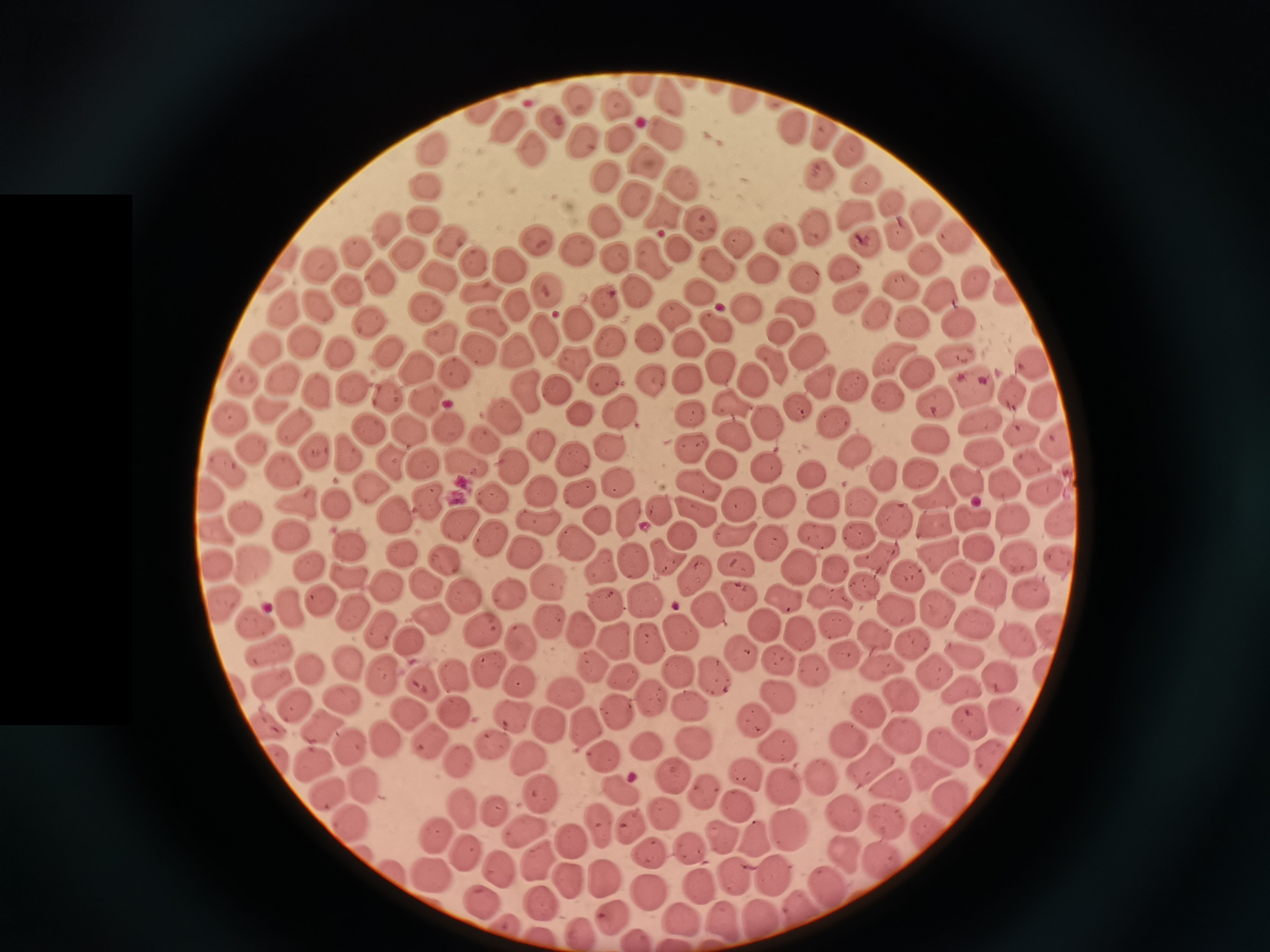

cell locations = approximate centers as (x, y) in pixels: (642, 82), (669, 97), (579, 98), (745, 102), (616, 105), (481, 108), (552, 118), (506, 124), (790, 127), (820, 130), (668, 133), (619, 139), (582, 140), (528, 145), (435, 149), (850, 151), (644, 162), (606, 175), (819, 176), (862, 177), (684, 178), (425, 187), (633, 196), (893, 204), (664, 212), (854, 215), (922, 216), (422, 220), (605, 220), (703, 221), (814, 224), (384, 228), (894, 233), (953, 238), (451, 240), (537, 242), (781, 242), (736, 243), (866, 243), (407, 246), (575, 248), (681, 248), (358, 251), (655, 258), (618, 259), (472, 261), (922, 261), (717, 262), (507, 263), (320, 265), (756, 265), (840, 270), (436, 274), (802, 278), (377, 279), (977, 285), (347, 286), (902, 286), (483, 290), (551, 290), (634, 291), (703, 291), (1007, 294), (942, 295), (605, 300), (849, 300), (517, 302), (747, 304), (315, 306), (428, 307), (285, 308), (797, 312), (674, 315), (878, 315), (485, 318), (371, 319), (959, 319), (915, 320), (579, 321), (718, 328), (780, 328), (542, 332), (444, 337), (651, 338), (306, 340), (683, 340), (610, 342), (389, 347), (519, 348), (270, 350), (480, 350), (343, 352), (809, 354), (955, 356), (892, 358), (769, 360), (572, 361), (418, 363), (1032, 363), (718, 364), (454, 368), (913, 371), (686, 376), (603, 378), (282, 380), (649, 380), (755, 380), (245, 381), (820, 381), (853, 386), (312, 387), (353, 388), (527, 388), (972, 388), (559, 390), (1012, 390), (886, 395), (384, 396), (1046, 396), (424, 397), (730, 401), (933, 404), (581, 409), (273, 411), (689, 411), (799, 411), (617, 413), (234, 415), (505, 418), (763, 420), (980, 422), (836, 423), (447, 427), (294, 428), (366, 428), (406, 430), (1020, 431), (732, 436), (489, 440), (689, 440), (539, 441), (607, 441), (936, 444), (1057, 447), (251, 449), (853, 451), (311, 453), (981, 453), (350, 456), (569, 457), (1027, 460), (460, 461), (393, 463), (422, 463), (512, 464), (720, 464), (766, 468), (227, 470), (281, 471), (917, 471), (810, 473), (885, 475), (964, 475), (614, 479), (698, 483), (370, 487), (1005, 487), (577, 489), (539, 490), (935, 494), (207, 495), (1044, 495), (491, 496), (776, 499), (431, 501), (294, 502), (739, 502), (863, 503), (335, 506), (659, 506), (696, 506), (821, 506), (398, 514), (628, 514), (596, 517), (245, 518), (536, 518), (894, 518), (1061, 518), (971, 519), (1014, 519), (932, 521), (458, 522), (215, 530), (861, 532), (733, 534), (287, 535), (683, 535), (817, 537), (492, 538), (573, 539), (765, 540), (348, 542), (977, 546), (524, 549), (937, 550), (666, 552), (1017, 552), (399, 553), (881, 557), (631, 558), (1058, 558), (441, 560), (253, 563), (304, 564), (602, 565), (732, 565), (217, 566), (798, 567), (833, 567), (904, 573), (693, 575), (962, 577), (353, 578), (546, 581), (422, 585), (387, 588), (994, 588), (508, 594), (733, 594), (641, 595), (781, 596), (460, 597), (1030, 598), (320, 599), (833, 599), (290, 604), (602, 604), (933, 605), (226, 607), (892, 609), (707, 611), (349, 612), (548, 620), (252, 623), (430, 623), (764, 623), (831, 623), (974, 626), (579, 627), (383, 628), (489, 629), (1050, 631), (678, 632), (798, 632), (646, 635), (412, 638), (875, 638), (523, 641), (616, 641), (1017, 641), (914, 648), (734, 651), (838, 651), (959, 652), (266, 655), (775, 658), (487, 663), (349, 665), (1047, 666), (591, 667), (816, 667), (881, 667), (311, 669), (674, 671), (933, 671), (385, 672), (620, 674), (710, 674), (454, 675), (269, 681), (517, 682), (1005, 682), (423, 684), (646, 688), (964, 688), (565, 690), (896, 695), (782, 697), (687, 701), (291, 702), (342, 703), (865, 708), (618, 709), (456, 712), (510, 712), (411, 713), (1006, 716), (755, 721), (549, 722), (583, 722), (972, 722), (316, 724), (267, 726), (902, 734), (693, 738), (387, 740), (493, 742), (850, 743), (944, 743), (348, 744), (652, 744), (427, 745), (777, 747), (529, 754), (600, 756), (992, 757), (277, 759), (314, 759), (459, 760), (868, 763), (666, 770), (923, 770), (747, 773), (822, 778), (617, 782), (784, 784), (889, 785), (362, 786), (534, 788), (705, 789), (326, 790), (950, 797), (735, 800), (462, 809), (498, 810), (662, 811), (844, 814), (599, 819), (886, 821), (349, 822), (630, 823), (521, 825), (785, 826), (930, 827), (435, 832), (722, 833), (567, 836), (759, 837), (688, 845), (463, 851), (646, 851), (843, 853), (882, 854), (539, 860), (499, 869), (396, 871), (775, 874), (738, 875), (430, 876), (602, 878), (698, 880), (824, 884), (570, 885), (648, 888), (480, 902), (542, 903), (799, 903), (681, 915), (608, 916), (761, 916), (724, 920), (576, 928), (633, 936), (672, 942)
capture = smartphone through the microscope eyepiece
image size = 1270×952 pixels
stain = Giemsa
field of view = single
preparation = thin smear